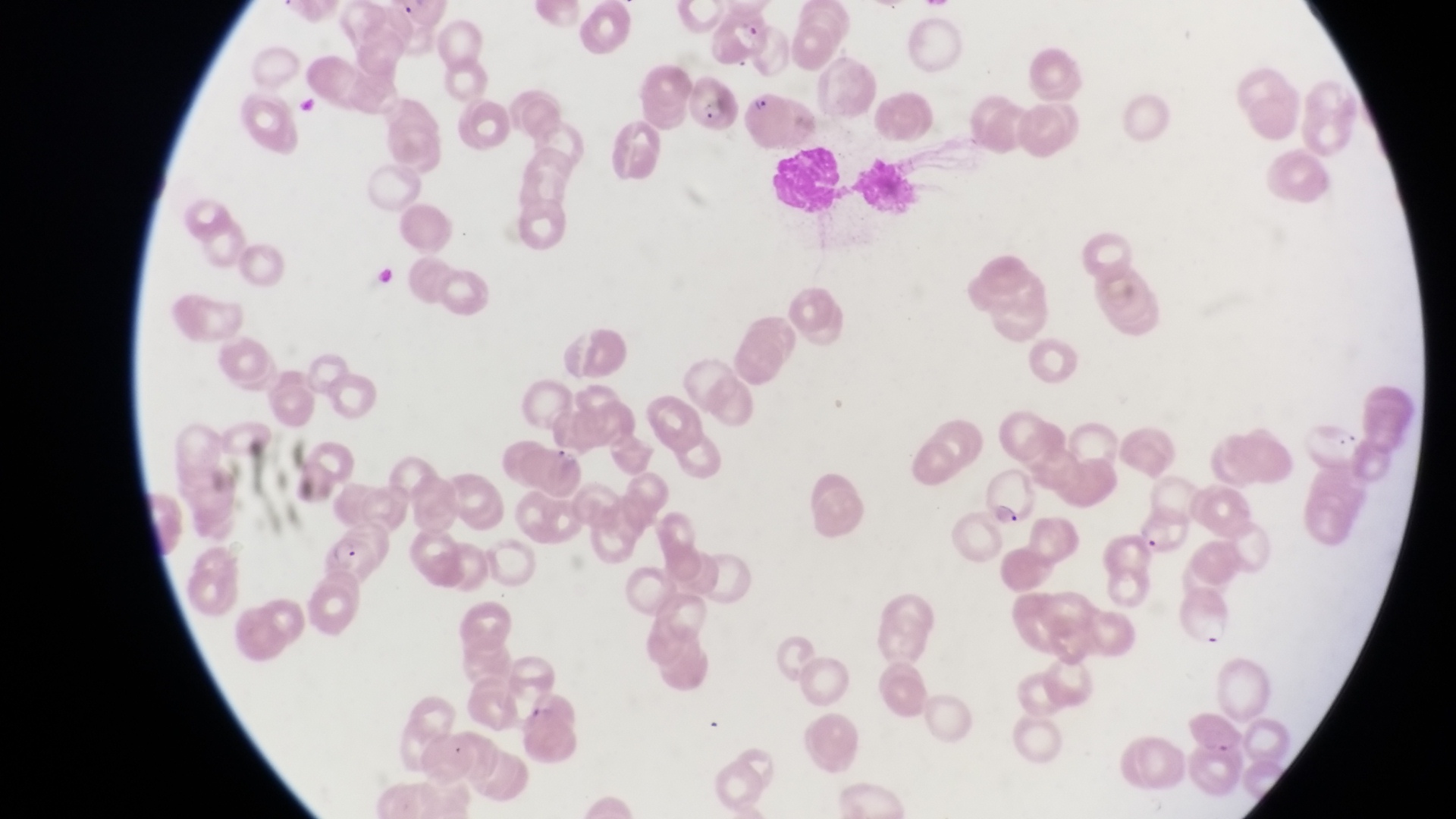

{
  "preparation": "thin blood film",
  "leukocyte_locations": "approximate bounding boxes as left top right bottom in pixels: 770 149 844 210; 853 157 925 225",
  "image_size": "1456×819 pixels",
  "parasitised_red_blood_cell_locations": "approximate bounding boxes as left top right bottom in pixels: 690 77 745 135; 748 89 795 152; 987 465 1034 526; 1141 515 1187 558; 315 532 374 581",
  "country": "Uganda",
  "magnification": "1000x",
  "capture": "smartphone photograph through the eyepiece of an Olympus CX-23 microscope",
  "field_of_view": "single"
}